Draw a bounding box around every trophozoite.
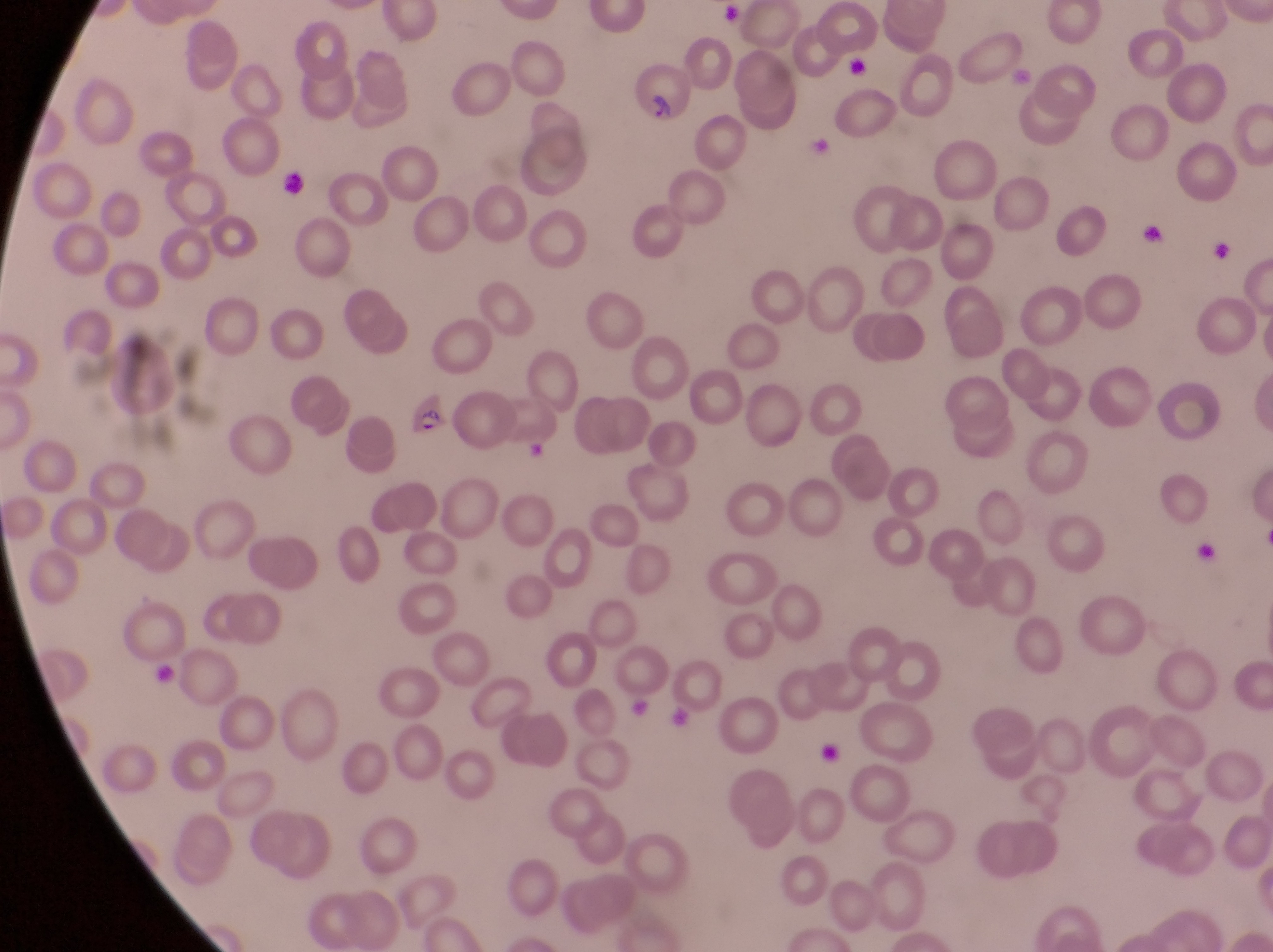
Approximate bounding boxes as left top right bottom in pixels.
Trophozoites: 1204 234 1232 269.

Summary:
  - Artifact (platelet-like body, stain precipitate, or debris) locations: 841 53 878 88; 275 170 315 203; 1136 212 1163 249; 1191 539 1219 572; 148 664 190 696; 817 734 849 766
  - Parasitised red blood cell locations: 629 58 691 128; 405 394 450 441
  - Image size: 1273×952 pixels
  - Magnification: 1000x
  - Preparation: thin blood smear
  - Country: Uganda
  - Field of view: single
  - Capture: smartphone photograph through the eyepiece of an Olympus CX-23 microscope